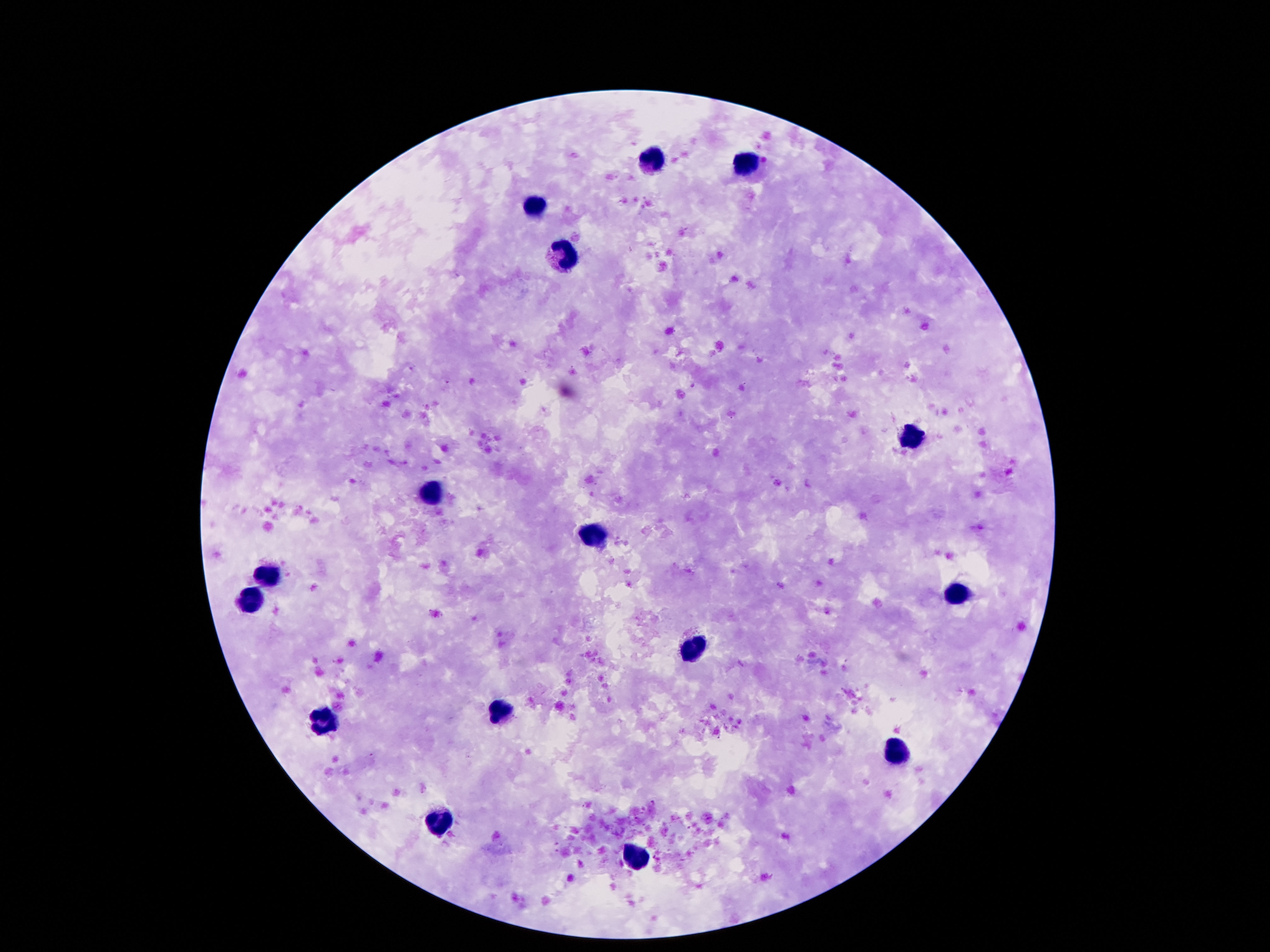

{
  "image_size": "1270×952 pixels",
  "stain": "Giemsa",
  "field_of_view": "single",
  "leukocyte_locations": "approximate centers as (x, y) in pixels: (651, 161), (749, 161), (535, 204), (563, 256), (908, 441), (433, 488), (590, 537), (270, 576), (951, 594), (249, 601), (692, 647), (493, 712), (322, 723), (898, 751), (442, 823), (638, 855)",
  "patient_malaria_status": "uninfected",
  "capture": "smartphone camera through the microscope eyepiece",
  "preparation": "thick peripheral-blood smear",
  "magnification": "100x"
}